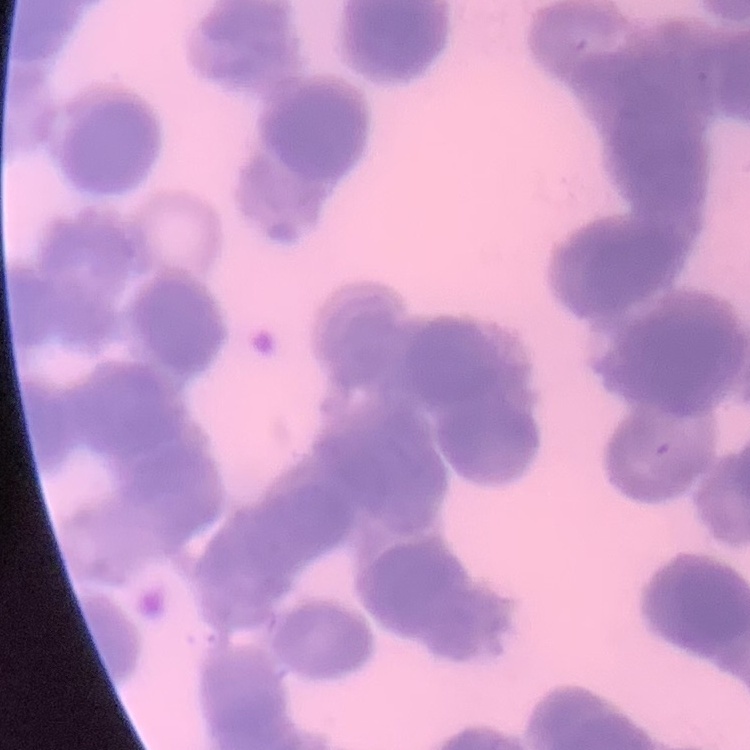
erythrocyte morphology = rouleaux formation
preparation = thin blood smear
stain = Field's or Giemsa
image type = square crop of a larger photomicrograph